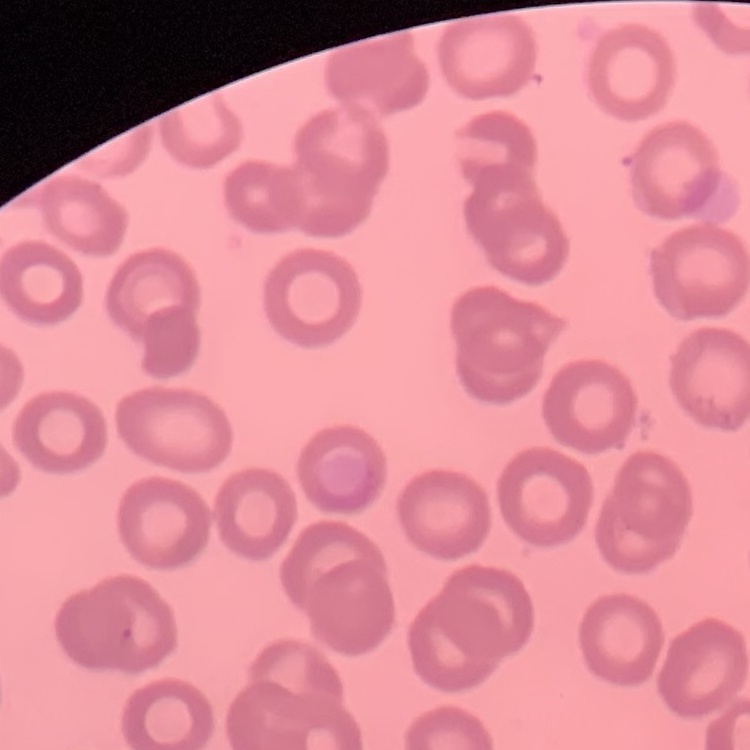

The red blood cells show no rouleaux formation. One tile cut from a larger photomicrograph. Thin blood smear. Stained with either Field's or Giemsa.